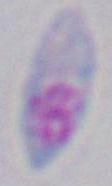
Photomicrograph. Toxoplasma gondii is shown. Captured at 1000x magnification.